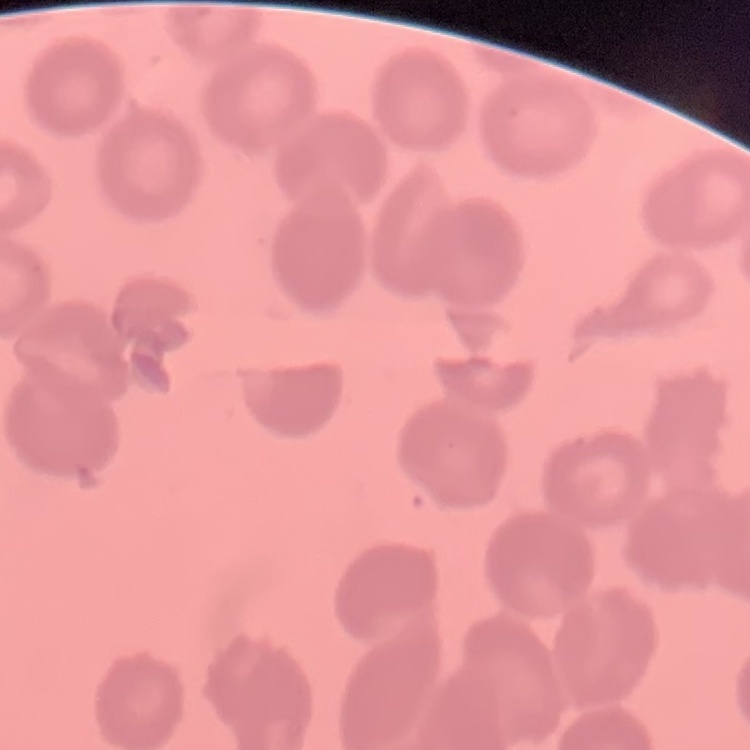

{
  "erythrocyte_morphology": "no rouleaux formation",
  "image_type": "one tile cut from a larger photomicrograph",
  "preparation": "thin blood smear",
  "stain": "Field's or Giemsa"
}